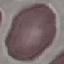 Result: negative for malaria parasites. Cell patch, automatically extracted from a larger field of view and resized to 64 × 64 pixels. Photographed with a smartphone camera at the microscope eyepiece. Giemsa-stained preparation. Thin smear of blood.